Give the position of every malaria parasite.
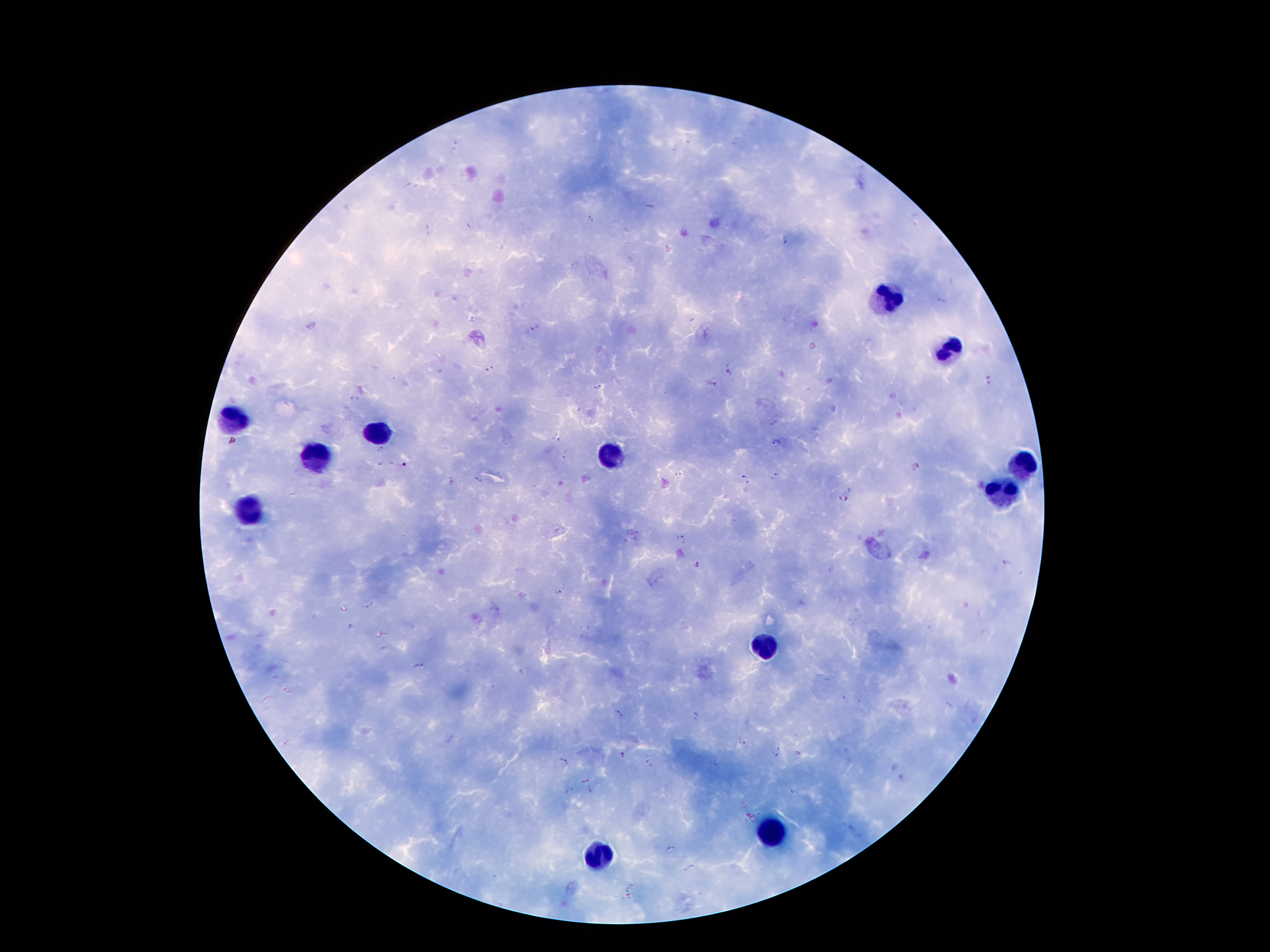

Approximate centers as [x, y] in pixels.
Malaria parasites: [689, 143], [735, 143], [675, 148], [590, 220], [784, 240], [575, 265], [940, 300], [472, 319], [538, 326], [490, 369], [729, 369], [987, 381], [713, 384], [597, 385], [355, 398], [774, 422], [557, 438], [777, 443], [382, 448], [565, 455], [380, 462], [392, 464], [405, 465], [915, 467], [680, 473], [774, 474], [747, 478], [478, 480], [453, 482], [840, 499], [849, 499], [680, 538], [1006, 562], [698, 564], [558, 591], [367, 603], [351, 626], [417, 665], [522, 671], [845, 699], [619, 715], [697, 715], [450, 739], [742, 741], [797, 754], [623, 755], [774, 756], [647, 759], [563, 762], [718, 764], [590, 790], [568, 791], [793, 793], [671, 851], [688, 868].

Leukocyte locations: [887, 301], [948, 349], [227, 420], [377, 433], [614, 458], [311, 460], [1021, 465], [1004, 496], [244, 513], [767, 643], [776, 834], [600, 855]. Giemsa-stained preparation. 100x magnification. Thick blood film. Single field of view. Photographed through the microscope eyepiece with a smartphone camera. Patient malaria status: infected with Plasmodium falciparum. Image is 1270×952 pixels.